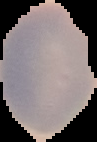
Summary:
  - Image type: segmented cell region on a black background
  - Preparation: thin blood smear
  - Image size: 97×142 pixels
  - Result: no Plasmodium parasites seen